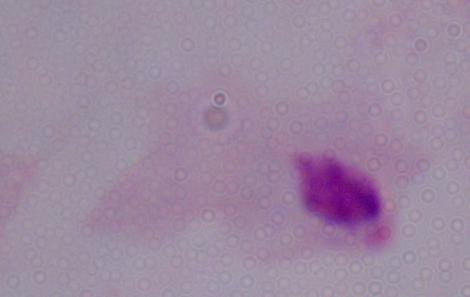
modality = micrograph
magnification = 1000x
identification = trichomonad